Classify this cell by malaria status.
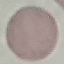

Uninfected.

Summary:
  - Stain: Giemsa
  - Image type: automatically extracted cell patch, resized to 64 × 64 pixels
  - Capture: smartphone camera at the microscope eyepiece
  - Preparation: thin smear